Name the blood parasite species.
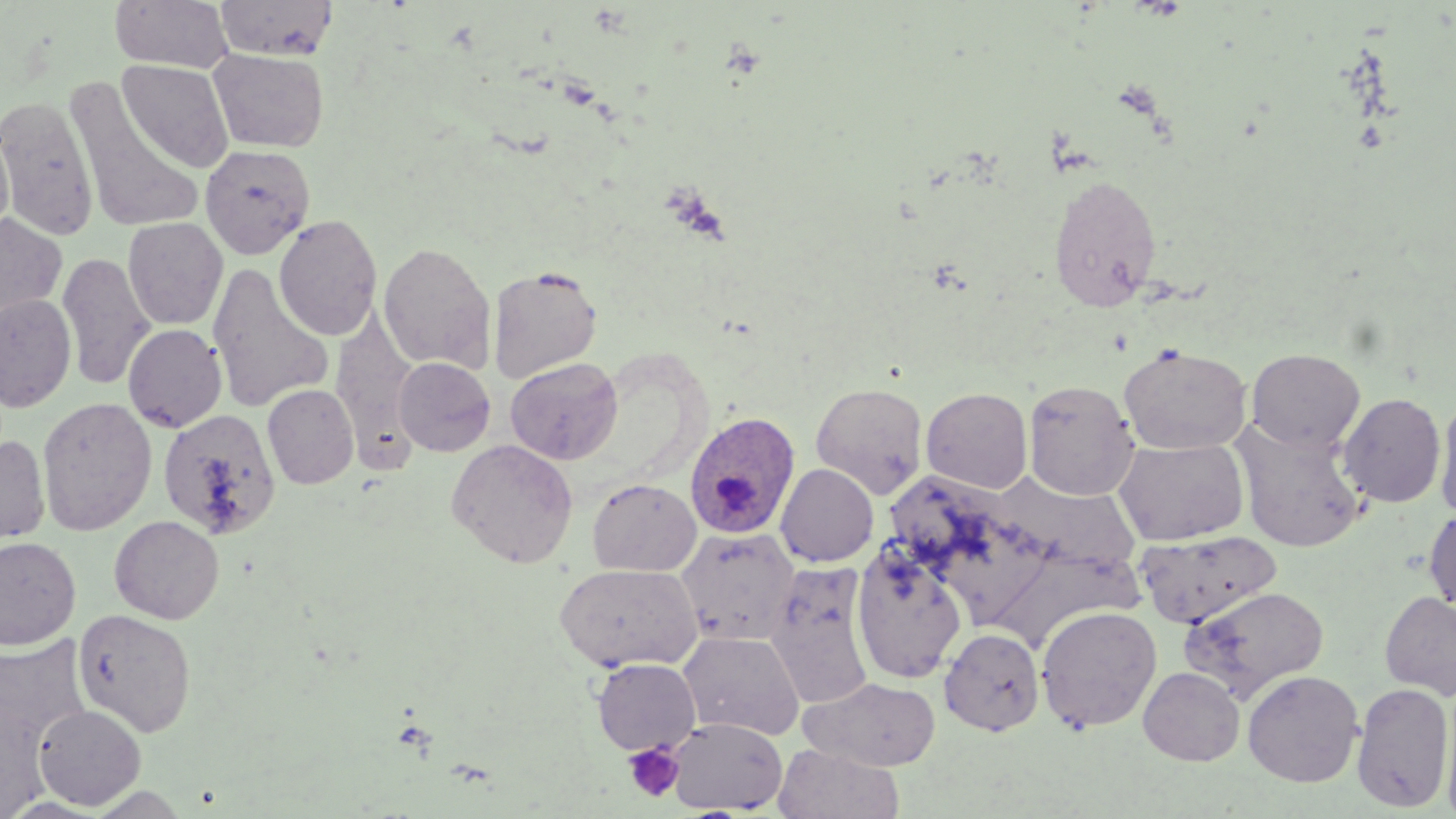
Plasmodium ovale.

Summary:
  - Coordinate format: approximate bounding boxes as (x1,y1)-(x2,y2) corner pairs in pixels
  - Plasmodium ovale-infected red blood cell locations: (683,411)-(800,540)
  - Platelet locations: (623,743)-(685,802)
  - Uninfected red blood cell locations: (110,0)-(232,73), (215,0)-(338,60), (208,49)-(329,153), (117,59)-(234,173), (64,76)-(203,233), (0,95)-(98,240), (0,121)-(14,246), (200,144)-(316,259), (1049,173)-(1162,311), (0,213)-(67,325), (274,214)-(382,341), (123,217)-(228,330), (378,242)-(496,373), (57,252)-(155,391), (208,263)-(334,414), (488,265)-(603,382), (0,294)-(77,412), (331,316)-(419,450), (123,324)-(227,432), (1118,344)-(1252,454), (1246,348)-(1365,453), (393,357)-(496,456), (505,357)-(623,465), (1023,378)-(1140,500), (810,382)-(930,499), (262,384)-(359,489), (921,387)-(1033,494), (1338,392)-(1446,508), (1435,395)-(1456,521), (37,397)-(157,536), (154,407)-(280,540), (1233,421)-(1367,552), (0,433)-(51,548), (1113,437)-(1249,545), (446,438)-(579,568), (775,463)-(878,566), (586,478)-(702,577), (1424,506)-(1456,614), (110,515)-(224,624), (675,527)-(801,646), (1135,531)-(1283,627), (0,536)-(81,650), (851,543)-(967,684), (554,562)-(703,673), (764,565)-(876,709), (1181,585)-(1329,699), (1380,591)-(1456,700), (1035,605)-(1163,732), (73,608)-(197,737), (939,627)-(1044,735), (678,630)-(804,740), (1,633)-(93,760), (591,657)-(702,755), (1139,666)-(1245,766), (1242,670)-(1363,787), (802,676)-(941,771), (1351,681)-(1454,812), (1439,689)-(1456,819), (33,704)-(147,810), (666,717)-(787,814), (773,742)-(904,819), (84,785)-(194,817)
  - Field of view: single
  - Image size: 1456×819 pixels
  - Modality: optical microscopy
  - Stain: May-Grünwald-Giemsa
  - Preparation: thin blood smear
  - Magnification: 1000x